Name the cell type shown.
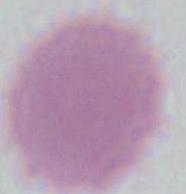

An erythrocyte.

modality = photomicrograph
magnification = 1000x